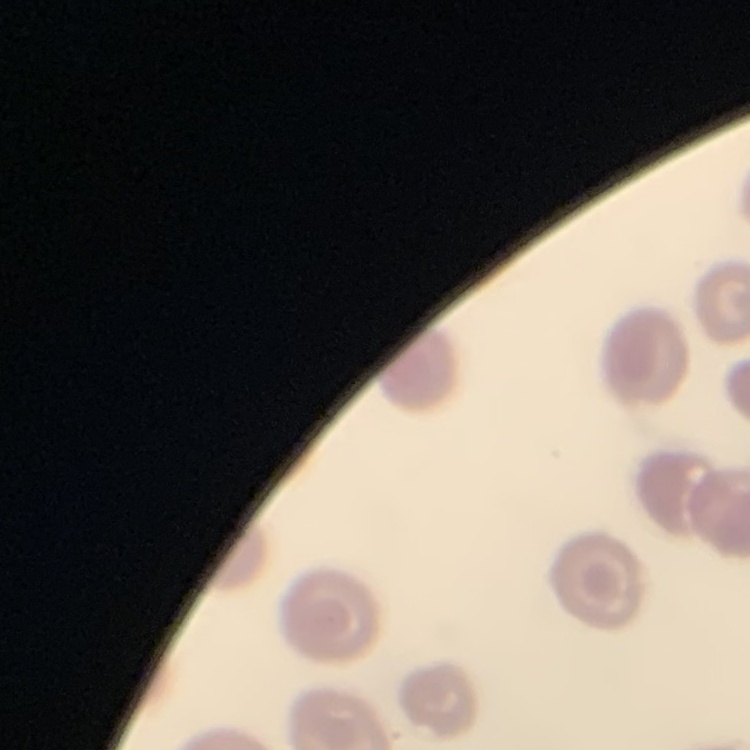 The erythrocytes show no rouleaux formation. Stained with either Field's or Giemsa. Thin blood film. Square crop of a larger photomicrograph.